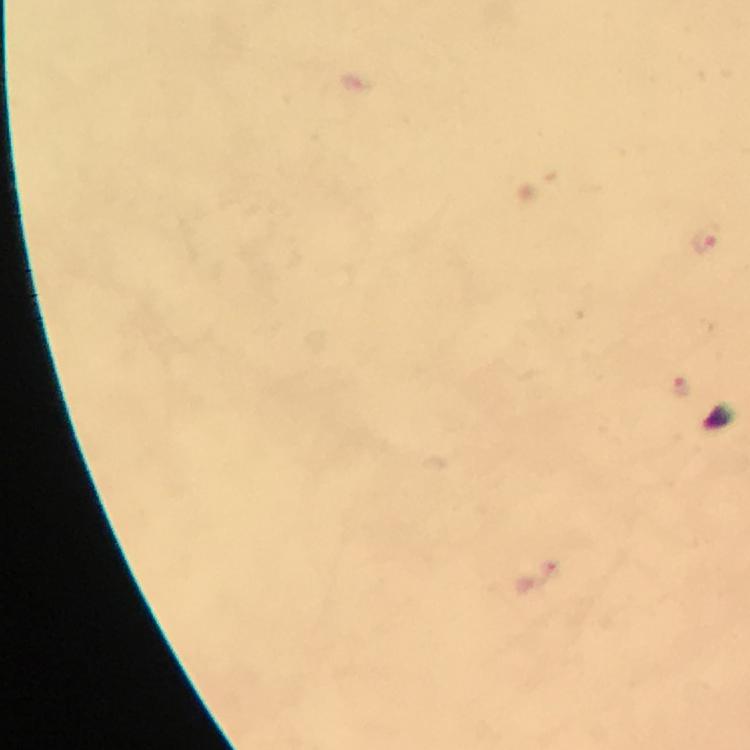

Approximate object centers, in pixels from the top-left corner.
Summary:
  - Malaria parasite locations: (x=708, y=238), (x=682, y=389)
  - Immersion oil: used
  - Cropped from: a single field of view
  - Context: from a malaria diagnostic workup
  - Stain: Giemsa
  - Magnification: 100x
  - Image size: 750×750 pixels
  - Preparation: thick smear
  - Capture: smartphone camera through the microscope